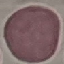
Summary:
  - Malaria status: uninfected
  - Capture: smartphone camera at the microscope eyepiece
  - Image type: automatically extracted cell patch, resized to 64 × 64 pixels
  - Preparation: thin blood smear
  - Stain: Giemsa